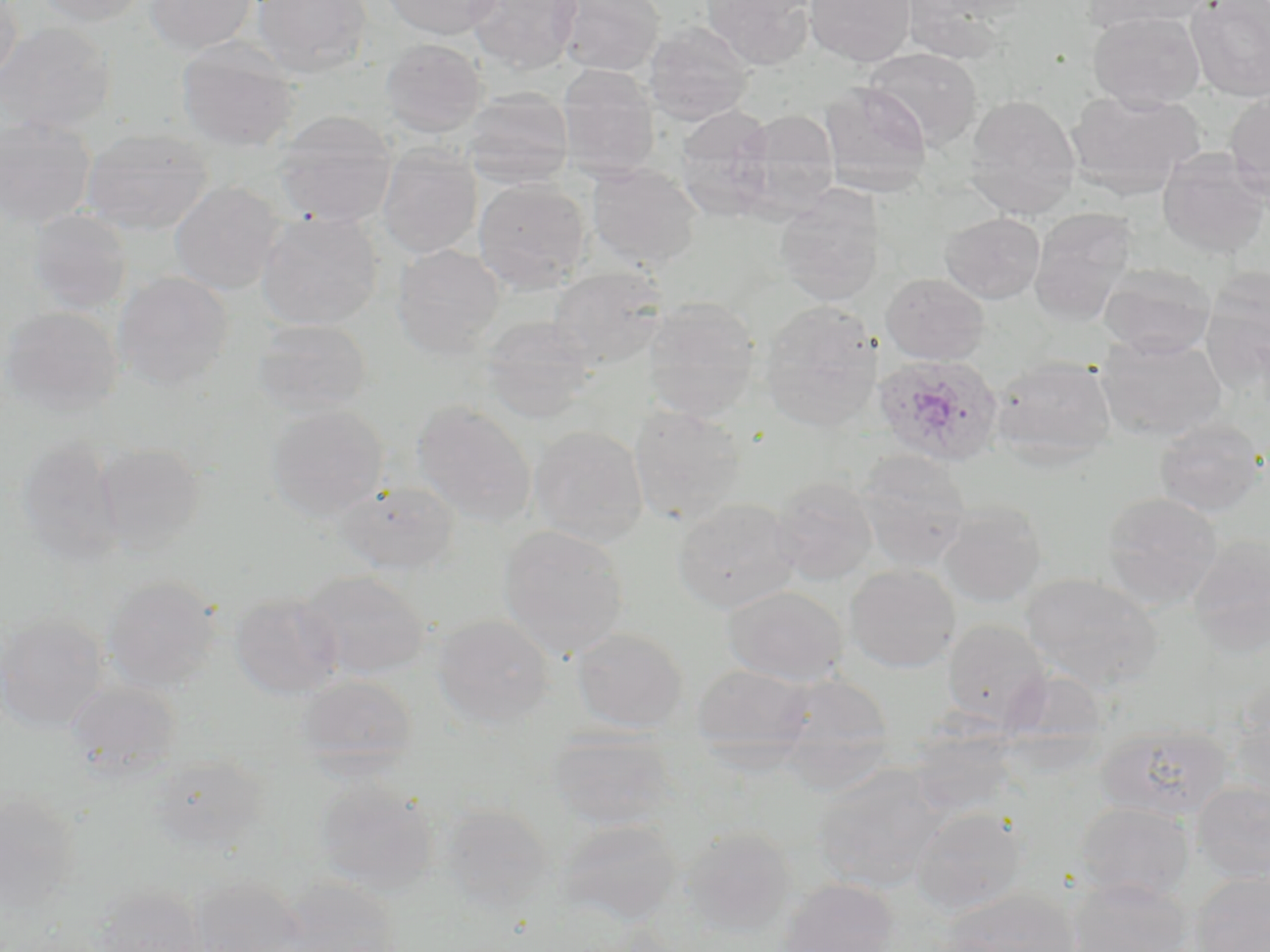
Approximate bounding boxes as (x1,y1)-(x2,y2) corner pairs in pixels. Uninfected red blood cell locations: (0,0)-(24,89), (34,0)-(147,27), (144,0)-(257,56), (251,0)-(372,77), (381,0)-(503,40), (465,0)-(582,74), (552,0)-(664,76), (701,0)-(815,70), (804,0)-(915,67), (1082,0)-(1212,32), (1186,0)-(1270,102), (897,1)-(1023,61), (1088,11)-(1205,111), (644,21)-(755,125), (0,22)-(115,136), (176,38)-(300,152), (380,38)-(488,137), (866,48)-(982,148), (557,64)-(660,180), (820,82)-(932,196), (461,88)-(574,189), (1066,89)-(1205,197), (1224,90)-(1270,200), (964,94)-(1081,218), (674,105)-(777,220), (274,110)-(398,227), (738,110)-(839,218), (0,114)-(96,229), (81,127)-(213,236), (376,145)-(482,258), (1157,151)-(1270,259), (586,162)-(703,271), (473,178)-(591,293), (169,181)-(284,295), (774,188)-(884,306), (1029,208)-(1140,325), (27,209)-(132,314), (256,211)-(384,330), (940,212)-(1045,304), (391,244)-(505,358), (1098,264)-(1216,358), (548,266)-(668,369), (1200,269)-(1270,392), (112,271)-(234,391), (881,273)-(989,365), (642,297)-(760,421), (759,300)-(883,431), (1,307)-(123,417), (479,315)-(597,423), (250,318)-(374,418), (1097,333)-(1227,441), (990,355)-(1118,467), (413,400)-(536,526), (266,404)-(389,520), (628,405)-(747,527), (1154,418)-(1266,517), (528,425)-(648,546), (15,435)-(124,567), (96,443)-(205,556), (855,449)-(973,570), (770,476)-(879,585), (335,480)-(460,574), (1100,491)-(1223,609), (672,497)-(801,613), (938,500)-(1047,607), (498,524)-(630,660), (1186,533)-(1270,657), (844,564)-(960,672), (298,569)-(430,679), (1021,572)-(1163,690), (102,576)-(221,692), (723,586)-(849,686), (229,591)-(345,699), (0,613)-(109,734), (431,613)-(556,729), (942,619)-(1051,730), (571,627)-(689,733), (692,663)-(814,757), (1000,666)-(1112,764), (770,672)-(895,784), (294,675)-(417,772), (65,679)-(182,780), (1226,697)-(1270,804), (1095,722)-(1233,822), (908,725)-(1019,818), (547,729)-(678,831), (148,753)-(268,854), (810,765)-(949,893), (314,778)-(438,895), (1190,781)-(1270,883), (0,791)-(82,912), (1074,801)-(1195,903), (440,802)-(556,912), (910,806)-(1029,916), (556,818)-(683,926), (679,826)-(798,936), (1189,870)-(1270,952), (189,875)-(307,952), (1066,877)-(1192,952), (277,878)-(403,952), (778,878)-(899,952), (94,884)-(208,952), (940,888)-(1081,952). Plasmodium ovale-infected red blood cell locations: (873,353)-(1006,466). Slide-level diagnosis: Plasmodium ovale. Image is 1270×952 pixels. Light microscopy. May-Grünwald-Giemsa stain. Thin blood smear. One field of a larger specimen. 1000x magnification.